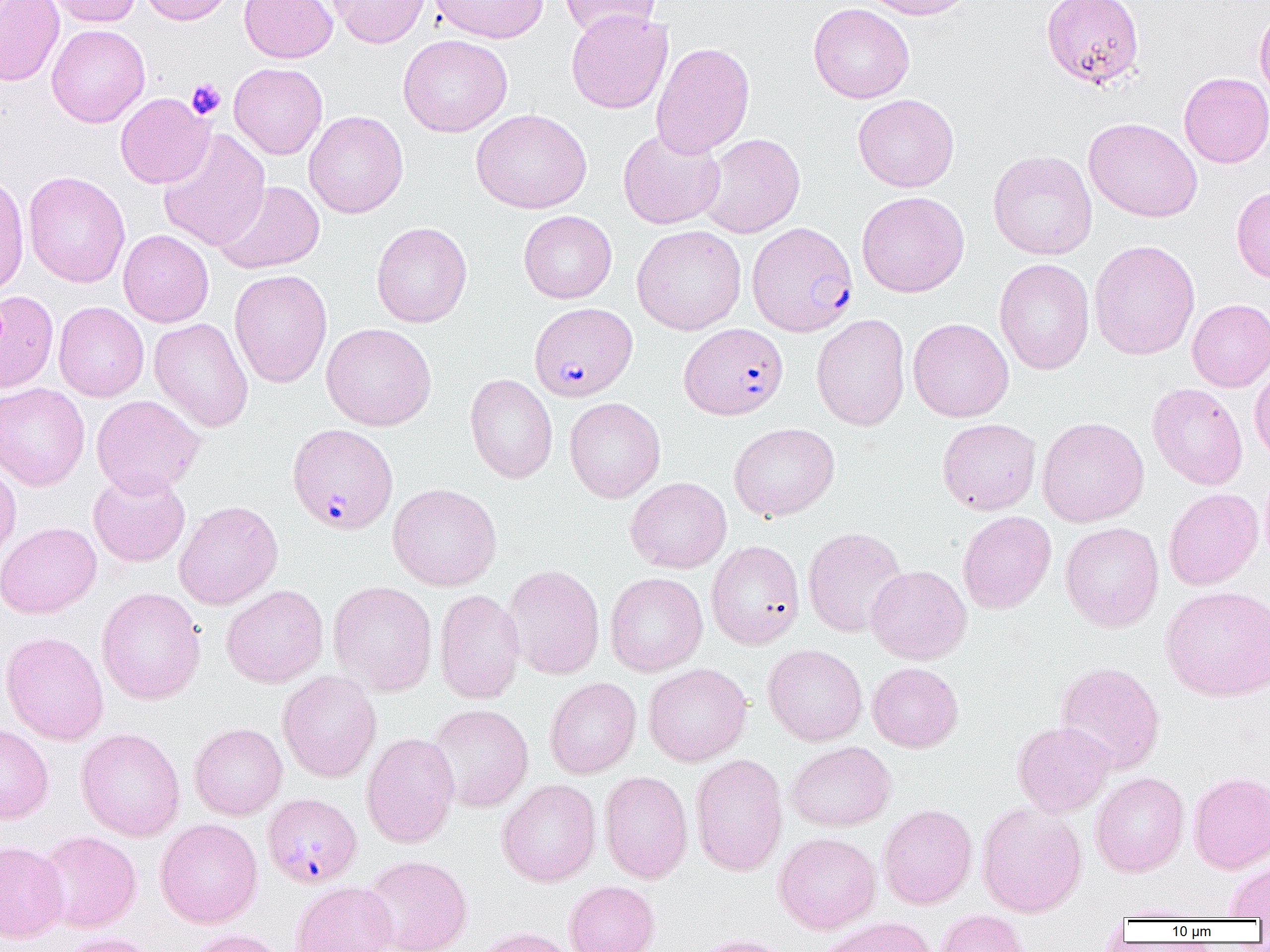

plasmodium_falciparum_infected_red_blood_cell_locations: 'approximate bounding boxes as (x1,y1)-(x2,y2) corner pairs in pixels: (747,222)-(858,337), (529,302)-(637,402), (679,322)-(789,420), (287,423)-(398,534), (262,793)-(362,888)'
slide_level_diagnosis: Plasmodium falciparum
platelet_locations: 'approximate bounding boxes as (x1,y1)-(x2,y2) corner pairs in pixels: (187,79)-(225,119)'
uninfected_red_blood_cell_locations: 'approximate bounding boxes as (x1,y1)-(x2,y2) corner pairs in pixels: (0,0)-(64,86), (41,0)-(141,27), (139,0)-(237,25), (239,0)-(337,63), (327,0)-(430,48), (428,0)-(548,43), (558,0)-(661,39), (858,0)-(978,20), (1041,0)-(1145,89), (808,3)-(915,104), (1254,7)-(1270,105), (566,9)-(673,114), (46,24)-(150,128), (398,34)-(512,137), (651,42)-(755,159), (229,63)-(328,159), (1179,72)-(1270,168), (115,93)-(214,188), (853,94)-(960,192), (471,109)-(592,214), (303,111)-(408,219), (1083,117)-(1202,223), (618,127)-(726,230), (157,128)-(270,252), (698,133)-(805,239), (988,150)-(1097,260), (23,171)-(130,287), (0,173)-(29,299), (214,180)-(325,274), (1231,186)-(1270,285), (857,191)-(969,298), (518,210)-(617,304), (371,221)-(472,328), (632,224)-(746,335), (118,230)-(214,327), (1089,240)-(1201,360), (994,258)-(1094,375), (229,269)-(332,388), (2,287)-(60,390), (1187,299)-(1270,392), (53,302)-(149,402), (55,310)-(252,409), (811,313)-(911,431), (149,318)-(253,433), (908,318)-(1014,422), (321,323)-(437,431), (1249,363)-(1270,462), (464,373)-(558,483), (0,382)-(90,491), (1147,383)-(1248,490), (91,395)-(205,497), (564,397)-(665,503), (1037,417)-(1149,527), (937,418)-(1042,514), (729,422)-(840,521), (0,462)-(21,565), (1260,465)-(1270,572), (88,470)-(190,567), (625,477)-(731,574), (387,483)-(502,591), (1163,488)-(1264,590), (173,500)-(283,610), (957,511)-(1056,614), (0,522)-(101,619), (1060,522)-(1164,632), (803,526)-(908,638), (706,540)-(805,649), (503,564)-(604,680), (865,565)-(972,665), (605,572)-(708,676), (328,581)-(438,695), (221,584)-(328,688), (1160,585)-(1270,702), (97,587)-(206,704), (435,589)-(525,704), (1,631)-(109,745), (763,644)-(867,746), (1055,661)-(1165,774), (867,662)-(963,752), (643,663)-(751,766), (278,670)-(382,783), (544,677)-(642,779), (427,704)-(534,812), (1012,721)-(1115,817), (189,722)-(287,820), (0,723)-(54,824), (76,728)-(185,841), (361,732)-(459,848), (786,741)-(896,831), (690,753)-(788,876), (598,770)-(693,884), (1188,771)-(1270,873), (1090,772)-(1189,877), (497,779)-(601,887), (976,803)-(1087,917), (878,804)-(978,909), (155,818)-(263,928), (36,830)-(142,933), (773,832)-(881,934), (0,840)-(69,942), (361,855)-(472,952), (1224,858)-(1270,919), (290,880)-(397,952), (564,880)-(660,952), (1110,903)-(1211,922), (935,909)-(1030,952), (815,917)-(938,952), (469,926)-(575,952), (183,928)-(289,952), (56,932)-(159,952), (691,934)-(794,952)'
image_size: 1270×952 pixels
field_of_view: one of a larger specimen
modality: light microscopy
magnification: 1000x
preparation: thin blood smear